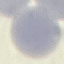

Malaria status: uninfected. Thin smear of blood. Acquired by smartphone through the microscope eyepiece. Giemsa stain. Automatically extracted cell patch, resized to 64 × 64 pixels.